Identify the parasite.
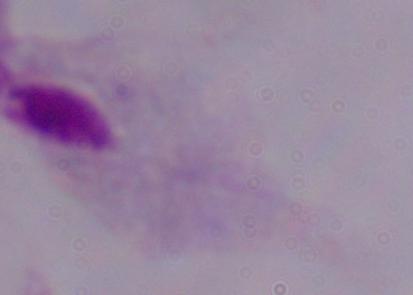
This is a trichomonad.

magnification = 1000x
modality = photomicrograph